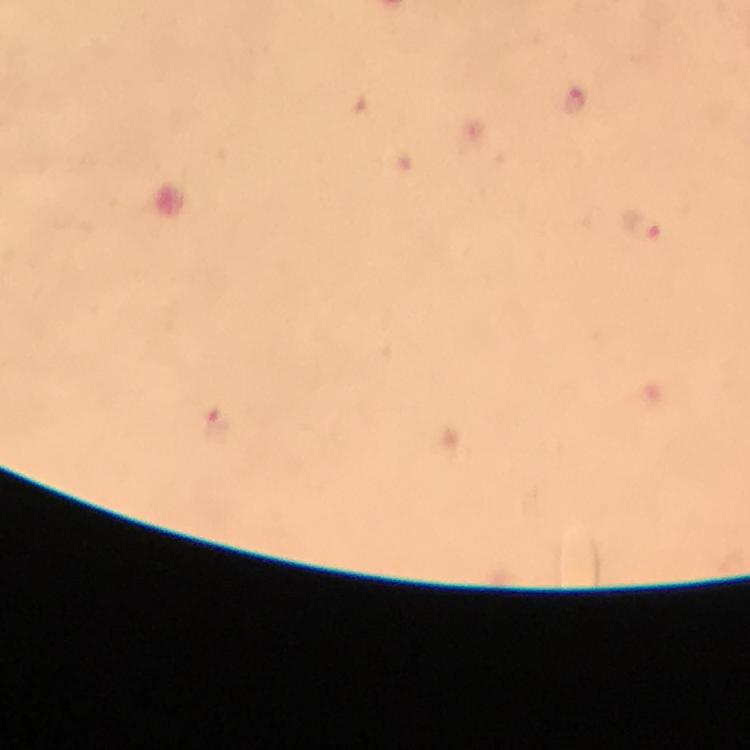 Approximate object centers, in pixels from the top-left corner. Malaria parasite locations: (x=576, y=102), (x=640, y=226), (x=216, y=426). At 100x magnification. A crop from one field of view. Thick smear. From a diagnostic examination for malaria. Image is 750×750 pixels. Photographed with a smartphone mounted on the microscope. Immersion oil applied. Giemsa stain.